Classify this cell by malaria status.
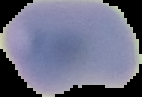

Uninfected.

Cell region segmented out of the field of view; the surrounding area is masked to black. From a thin blood smear. Image is 142×97 pixels.